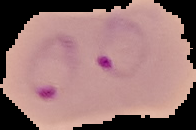

Segmented cell region on a black background. From a thin blood smear. Result: malaria parasites identified. Image is 196×130 pixels.